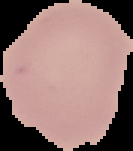

Summary:
  - Image size: 133×151 pixels
  - Image type: segmented cell region with the area outside set to black
  - Result: no Plasmodium parasites detected
  - Preparation: thin blood film